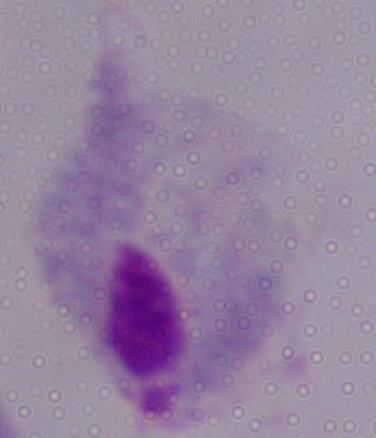

Summary:
  - Modality: photomicrograph
  - Identification: trichomonad
  - Magnification: 1000x